Classify this cell by malaria status.
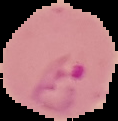
Parasitized.

Image is 118×121 pixels. From a thin blood smear. Segmented cell region on a black background.